Classify this cell by malaria status.
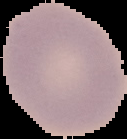
It is uninfected.

preparation = thin blood smear
image type = segmented cell region with the area outside set to black
image size = 127×139 pixels